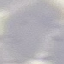

Result: no malaria parasites seen. Photographed with a smartphone camera at the microscope eyepiece. Thin smear of blood. Cell patch, automatically extracted from a larger field of view and resized to 64 × 64 pixels. Giemsa stain.